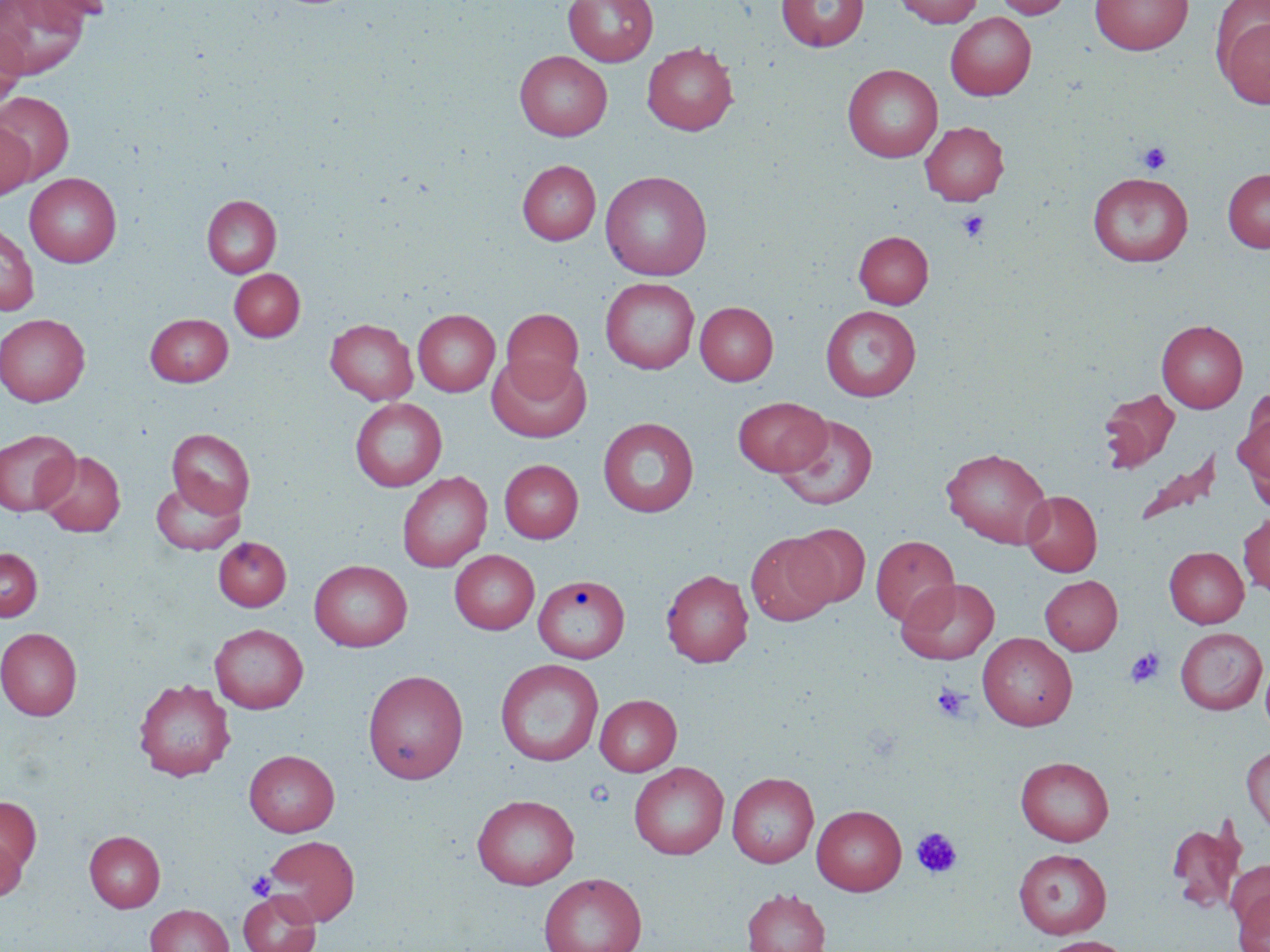

Approximate bounding boxes as (x1,y1)-(x2,y2) corner pairs in pixels. Platelet locations: (1138,142)-(1171,174), (956,210)-(989,243), (1125,647)-(1164,688), (932,684)-(971,722), (911,827)-(963,878), (246,870)-(277,900). Uninfected red blood cell locations: (23,0)-(114,24), (563,0)-(658,66), (777,0)-(868,51), (894,0)-(984,28), (995,0)-(1071,19), (1090,0)-(1193,55), (0,1)-(89,79), (1217,7)-(1270,111), (945,12)-(1036,100), (0,27)-(26,111), (642,42)-(738,135), (515,50)-(612,141), (843,63)-(943,162), (0,91)-(75,184), (920,121)-(1008,206), (0,122)-(34,200), (517,160)-(601,245), (1222,168)-(1270,253), (599,170)-(713,280), (24,172)-(122,267), (1088,173)-(1193,267), (202,195)-(281,278), (0,222)-(38,316), (853,230)-(933,308), (229,269)-(305,342), (600,277)-(700,374), (695,301)-(778,385), (820,305)-(921,401), (412,309)-(500,396), (501,309)-(584,395), (145,313)-(233,386), (0,314)-(90,406), (325,318)-(418,404), (1157,319)-(1248,413), (487,355)-(591,442), (1099,389)-(1179,472), (733,396)-(830,476), (350,398)-(447,491), (1234,403)-(1270,501), (775,414)-(879,510), (598,417)-(699,517), (166,428)-(255,517), (0,429)-(81,517), (941,446)-(1052,548), (37,450)-(125,537), (1134,451)-(1221,528), (499,459)-(583,543), (397,471)-(491,572), (151,478)-(246,554), (1021,490)-(1102,576), (1238,511)-(1270,598), (788,524)-(870,607), (746,532)-(837,626), (871,535)-(960,627), (213,537)-(291,611), (0,547)-(42,621), (1164,547)-(1249,628), (450,550)-(540,634), (309,560)-(413,652), (661,569)-(753,667), (533,575)-(629,663), (1040,575)-(1122,654), (896,577)-(999,664), (209,623)-(308,713), (0,627)-(82,720), (1175,627)-(1267,715), (978,633)-(1077,731), (1260,658)-(1270,736), (495,659)-(604,766), (363,669)-(469,784), (133,678)-(235,781), (595,694)-(682,776), (1242,744)-(1270,837), (244,750)-(340,836), (1015,756)-(1114,846), (629,762)-(729,859), (727,772)-(819,868), (471,793)-(580,890), (0,796)-(42,880), (812,804)-(907,895), (1166,815)-(1247,915), (84,830)-(165,912), (0,832)-(25,903), (263,835)-(360,926), (1013,848)-(1112,938), (1225,858)-(1270,936), (538,872)-(647,952), (741,888)-(830,952), (239,890)-(321,952), (1234,890)-(1270,952), (145,904)-(233,952), (1038,935)-(1132,952). Slide-level diagnosis: negative for blood parasites. Optical microscopy. One field of a larger specimen. 1000x magnification. Thin blood film. May-Grünwald-Giemsa-stained preparation. Image is 1270×952 pixels.